Point out each malaria parasite.
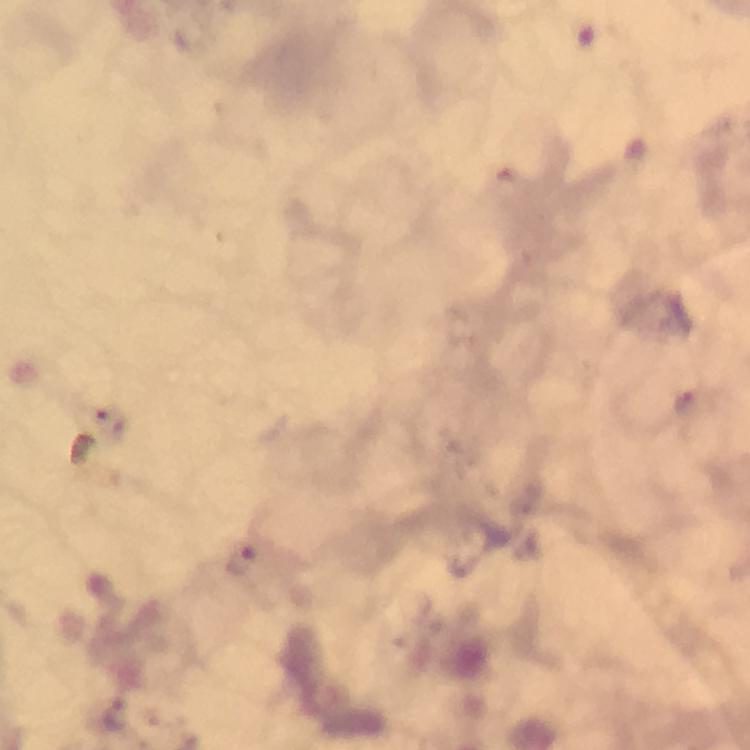
Approximate centers as [x, y] in pixels.
Malaria parasites: [241, 562], [119, 715].

image_size: 750×750 pixels
cropped_from: a single field of view
magnification: 100x
immersion_oil: applied
capture: smartphone photograph through a microscope
context: from a malaria diagnostic workup
stain: Giemsa
preparation: thick blood smear